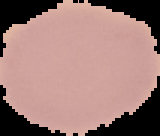

image_size: 160×136 pixels
malaria_status: uninfected
image_type: segmented cell region on a black background
preparation: thin blood smear